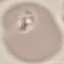
Result: no malaria parasites detected. Cell patch, automatically extracted from a larger field of view and resized to 64 × 64 pixels. Thin blood film. Photographed with a smartphone camera at the microscope eyepiece. Giemsa stain.